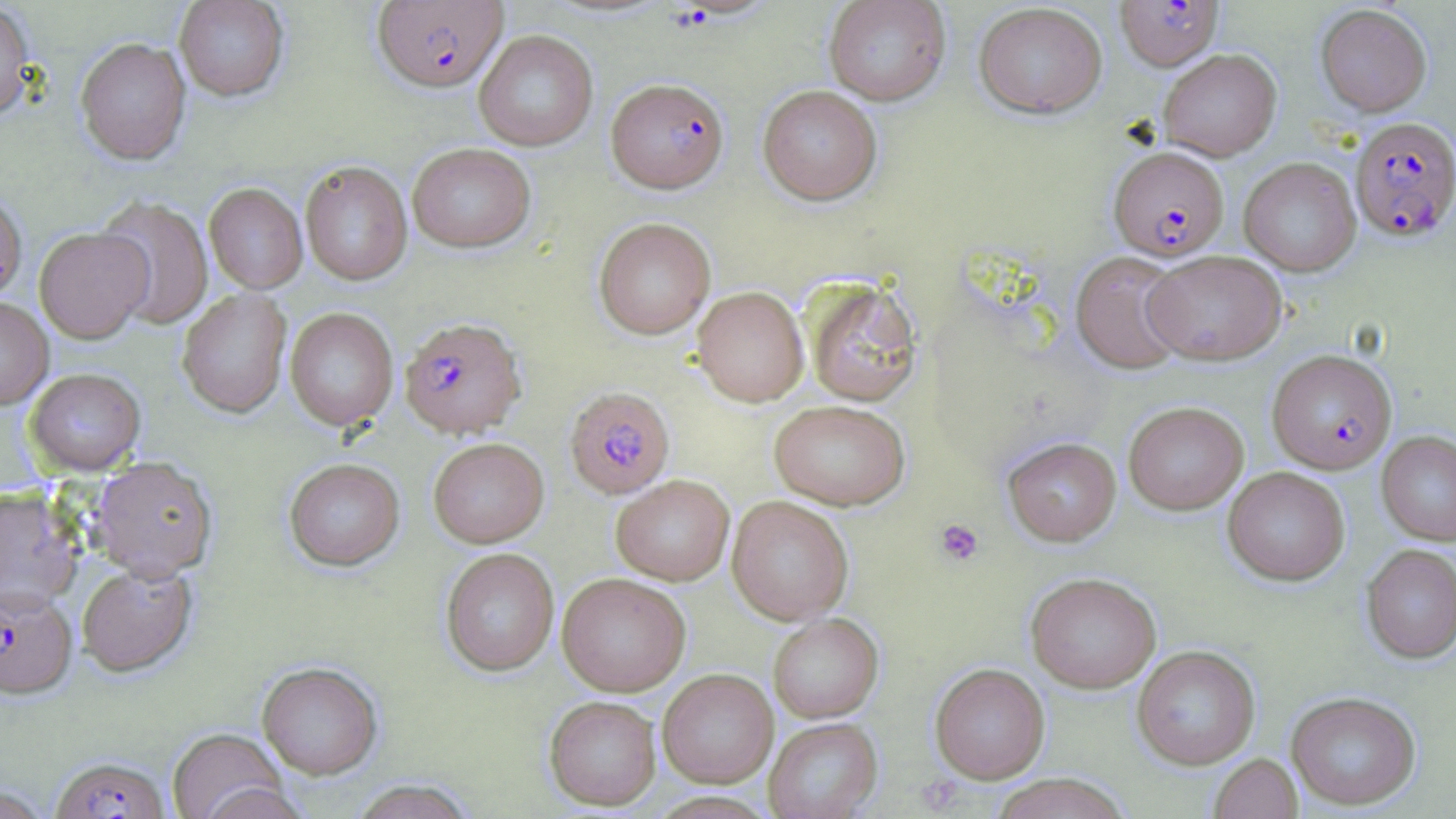

Summary:
  - Coordinate format: approximate bounding boxes as named x1/y1/x2/y2 corners in pixels
  - Uninfected red blood cell locations: (x1=173, y1=0, x2=290, y2=102), (x1=823, y1=0, x2=951, y2=105), (x1=973, y1=2, x2=1108, y2=119), (x1=0, y1=3, x2=36, y2=124), (x1=1315, y1=4, x2=1432, y2=116), (x1=473, y1=30, x2=598, y2=151), (x1=75, y1=37, x2=191, y2=165), (x1=1158, y1=48, x2=1282, y2=161), (x1=757, y1=85, x2=882, y2=205), (x1=407, y1=143, x2=536, y2=253), (x1=1238, y1=157, x2=1361, y2=276), (x1=299, y1=161, x2=413, y2=287), (x1=204, y1=183, x2=308, y2=294), (x1=0, y1=192, x2=27, y2=303), (x1=93, y1=195, x2=214, y2=331), (x1=593, y1=217, x2=716, y2=340), (x1=34, y1=227, x2=153, y2=345), (x1=1070, y1=250, x2=1190, y2=375), (x1=1143, y1=250, x2=1287, y2=365), (x1=802, y1=277, x2=924, y2=406), (x1=692, y1=286, x2=809, y2=407), (x1=176, y1=288, x2=292, y2=419), (x1=0, y1=298, x2=54, y2=410), (x1=284, y1=308, x2=398, y2=432), (x1=25, y1=370, x2=145, y2=477), (x1=768, y1=399, x2=911, y2=510), (x1=1123, y1=401, x2=1248, y2=514), (x1=1376, y1=431, x2=1456, y2=546), (x1=1002, y1=437, x2=1121, y2=546), (x1=428, y1=439, x2=549, y2=549), (x1=89, y1=458, x2=218, y2=583), (x1=284, y1=460, x2=405, y2=573), (x1=1222, y1=466, x2=1351, y2=586), (x1=611, y1=476, x2=734, y2=586), (x1=0, y1=489, x2=84, y2=613), (x1=726, y1=495, x2=854, y2=625), (x1=1360, y1=544, x2=1456, y2=663), (x1=440, y1=548, x2=559, y2=677), (x1=77, y1=565, x2=197, y2=680), (x1=1025, y1=571, x2=1161, y2=693), (x1=557, y1=573, x2=691, y2=697), (x1=768, y1=613, x2=883, y2=723), (x1=1131, y1=645, x2=1261, y2=770), (x1=257, y1=663, x2=383, y2=781), (x1=929, y1=663, x2=1050, y2=784), (x1=657, y1=669, x2=778, y2=788), (x1=1286, y1=691, x2=1422, y2=810), (x1=544, y1=698, x2=662, y2=812), (x1=764, y1=717, x2=882, y2=819), (x1=167, y1=730, x2=293, y2=819), (x1=1208, y1=753, x2=1303, y2=819), (x1=987, y1=774, x2=1132, y2=818), (x1=350, y1=780, x2=477, y2=819), (x1=1, y1=783, x2=54, y2=818)
  - Plasmodium falciparum-infected red blood cell locations: (x1=1115, y1=0, x2=1224, y2=71), (x1=372, y1=1, x2=507, y2=93), (x1=605, y1=78, x2=730, y2=194), (x1=1349, y1=116, x2=1456, y2=242), (x1=1109, y1=146, x2=1229, y2=261), (x1=399, y1=317, x2=526, y2=439), (x1=1266, y1=349, x2=1397, y2=473), (x1=564, y1=387, x2=675, y2=499), (x1=0, y1=589, x2=78, y2=703), (x1=50, y1=758, x2=171, y2=819)
  - Platelet locations: (x1=935, y1=519, x2=984, y2=567), (x1=916, y1=775, x2=964, y2=813)
  - Slide-level diagnosis: Plasmodium falciparum
  - Magnification: 1000x
  - Preparation: thin blood film
  - Field of view: one of a larger specimen
  - Stain: May-Grünwald-Giemsa
  - Modality: optical microscopy
  - Image size: 1456×819 pixels